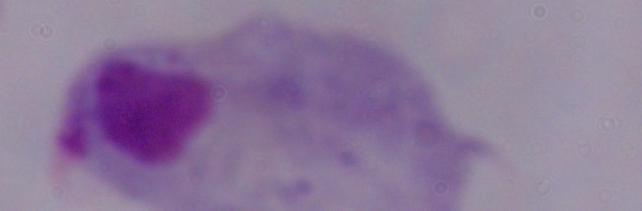 Photomicrograph. 1000x magnification. A trichomonad is shown.